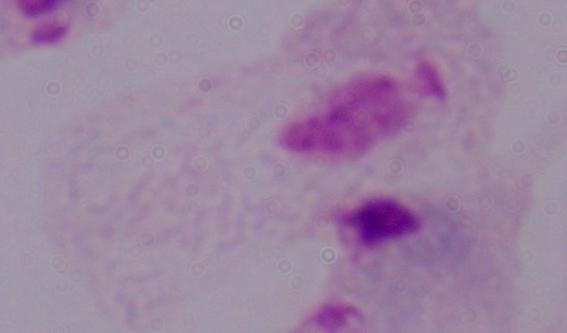

magnification: 1000x
modality: photomicrograph
identification: trichomonad